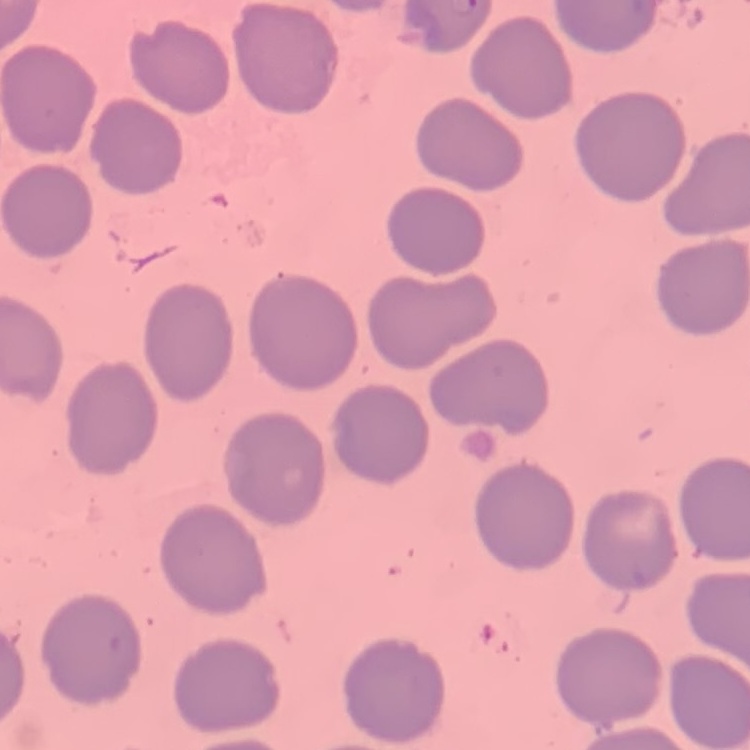
{
  "red_blood_cell_morphology": "no rouleaux formation",
  "image_type": "one tile cut from a larger photomicrograph",
  "stain": "Field's or Giemsa",
  "preparation": "thin blood smear"
}